Report the malaria status of this cell.
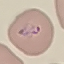

It is parasitized.

Summary:
  - Preparation: thin blood smear
  - Image type: cell patch, automatically extracted from a larger field of view and resized to 64 × 64 pixels
  - Capture: smartphone camera at the microscope eyepiece
  - Stain: Giemsa